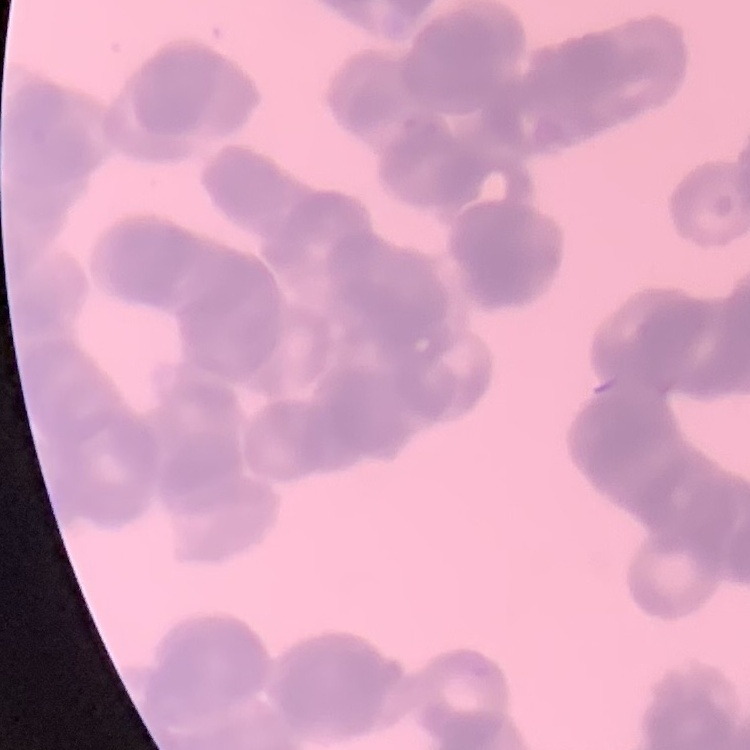

erythrocyte morphology = rouleaux formation
stain = Field's or Giemsa
preparation = thin peripheral smear
image type = one tile cut from a larger photomicrograph